Comment on the morphology of the erythrocytes.
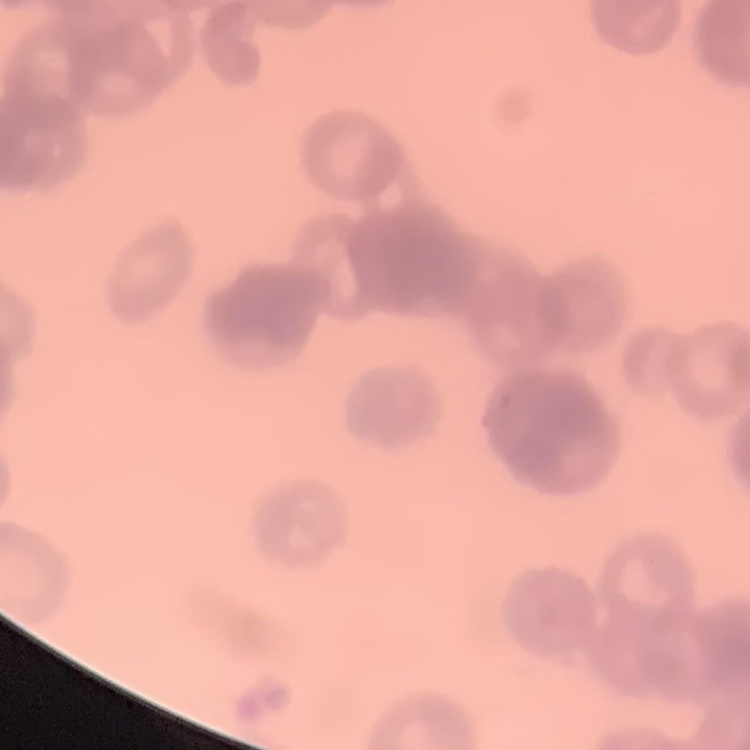

Rouleaux formation.

{
  "stain": "Field's or Giemsa",
  "image_type": "one tile cut from a larger photomicrograph",
  "preparation": "thin blood film"
}